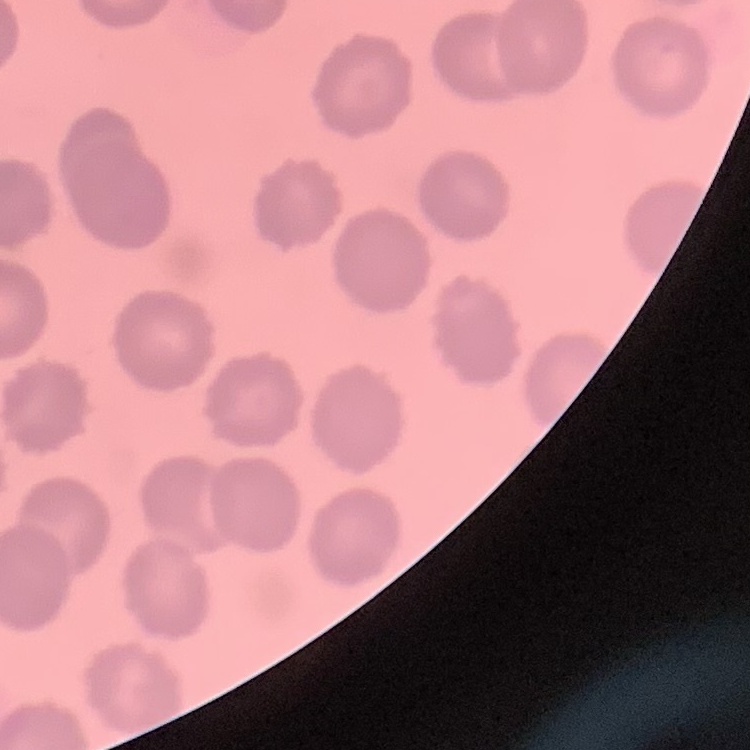

The erythrocytes show no rouleaux formation. Thin peripheral smear. Stained with either Field's or Giemsa. Square crop of a larger photomicrograph.